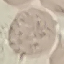
result: no malaria parasites seen
capture: smartphone through the microscope eyepiece
preparation: thin smear
stain: Giemsa
image_type: cell patch, automatically extracted from a larger field of view and resized to 64 × 64 pixels